Outline each uninfected red blood cell.
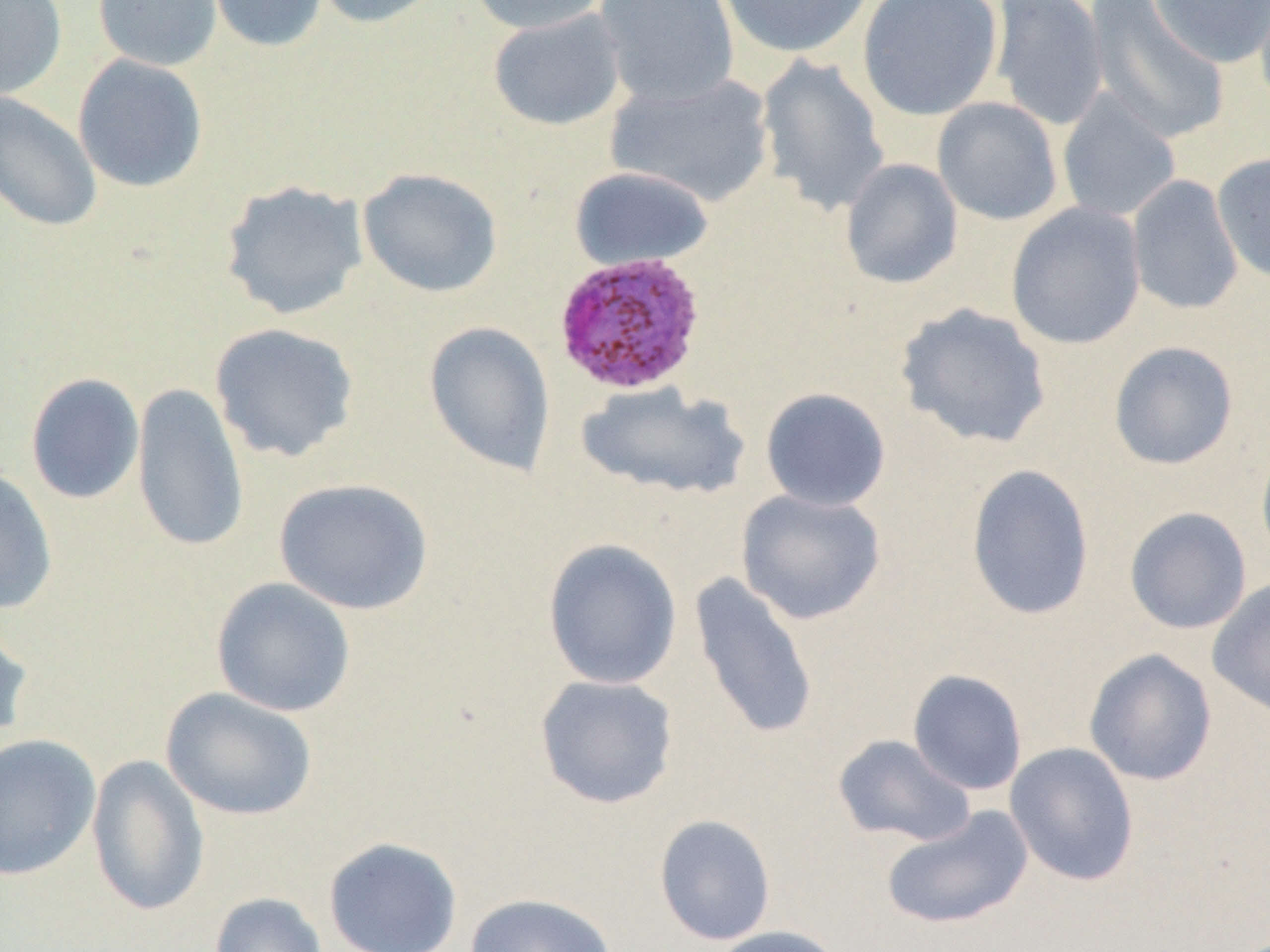

Approximate bounding boxes as named x1/y1/x2/y2 corners in pixels.
Uninfected red blood cells: (x1=0, y1=0, x2=68, y2=101), (x1=92, y1=0, x2=223, y2=71), (x1=204, y1=0, x2=328, y2=54), (x1=312, y1=0, x2=446, y2=29), (x1=467, y1=0, x2=612, y2=35), (x1=593, y1=0, x2=741, y2=108), (x1=716, y1=0, x2=874, y2=59), (x1=857, y1=0, x2=1003, y2=121), (x1=1083, y1=0, x2=1230, y2=145), (x1=1150, y1=0, x2=1270, y2=69), (x1=989, y1=1, x2=1109, y2=131), (x1=488, y1=9, x2=627, y2=131), (x1=72, y1=54, x2=209, y2=193), (x1=755, y1=55, x2=890, y2=215), (x1=605, y1=71, x2=775, y2=208), (x1=0, y1=91, x2=103, y2=232), (x1=1057, y1=91, x2=1181, y2=222), (x1=932, y1=97, x2=1063, y2=226), (x1=1212, y1=150, x2=1270, y2=284), (x1=839, y1=157, x2=963, y2=290), (x1=569, y1=166, x2=714, y2=272), (x1=357, y1=167, x2=504, y2=298), (x1=1127, y1=175, x2=1243, y2=316), (x1=219, y1=180, x2=369, y2=320), (x1=1006, y1=202, x2=1146, y2=349), (x1=894, y1=302, x2=1052, y2=450), (x1=423, y1=320, x2=556, y2=478), (x1=209, y1=322, x2=359, y2=463), (x1=1108, y1=340, x2=1239, y2=470), (x1=25, y1=372, x2=145, y2=505), (x1=132, y1=381, x2=249, y2=555), (x1=576, y1=382, x2=750, y2=501), (x1=760, y1=387, x2=891, y2=512), (x1=1256, y1=437, x2=1270, y2=571), (x1=965, y1=463, x2=1095, y2=621), (x1=0, y1=467, x2=59, y2=616), (x1=273, y1=477, x2=434, y2=615), (x1=735, y1=489, x2=887, y2=625), (x1=1123, y1=506, x2=1252, y2=635), (x1=542, y1=538, x2=683, y2=690), (x1=689, y1=572, x2=819, y2=740), (x1=210, y1=577, x2=357, y2=717), (x1=1207, y1=577, x2=1270, y2=719), (x1=0, y1=616, x2=33, y2=750), (x1=1083, y1=648, x2=1217, y2=786), (x1=907, y1=669, x2=1028, y2=796), (x1=534, y1=674, x2=679, y2=809), (x1=160, y1=687, x2=318, y2=822), (x1=0, y1=733, x2=102, y2=880), (x1=832, y1=734, x2=977, y2=847), (x1=1004, y1=742, x2=1140, y2=886), (x1=85, y1=753, x2=210, y2=917), (x1=879, y1=805, x2=1034, y2=931), (x1=653, y1=813, x2=777, y2=946), (x1=323, y1=836, x2=463, y2=952), (x1=208, y1=892, x2=328, y2=952), (x1=464, y1=892, x2=618, y2=952), (x1=710, y1=925, x2=845, y2=952).

slide-level diagnosis = Plasmodium ovale
preparation = thin blood smear
magnification = 1000x
Plasmodium ovale-infected red blood cell locations = approximate bounding boxes as named x1/y1/x2/y2 corners in pixels: (x1=553, y1=251, x2=707, y2=396)
image size = 1270×952 pixels
modality = light microscopy
field of view = single